Comment on the morphology of the erythrocytes.
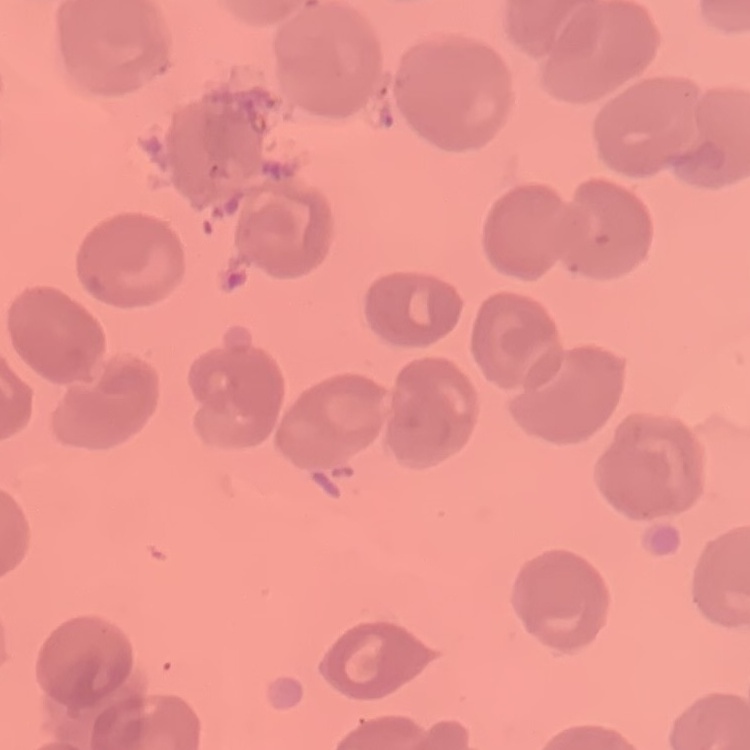

They show no rouleaux formation.

Summary:
  - Stain: Field's or Giemsa
  - Image type: square crop of a larger photomicrograph
  - Preparation: thin blood smear